Assess the morphology of the erythrocytes.
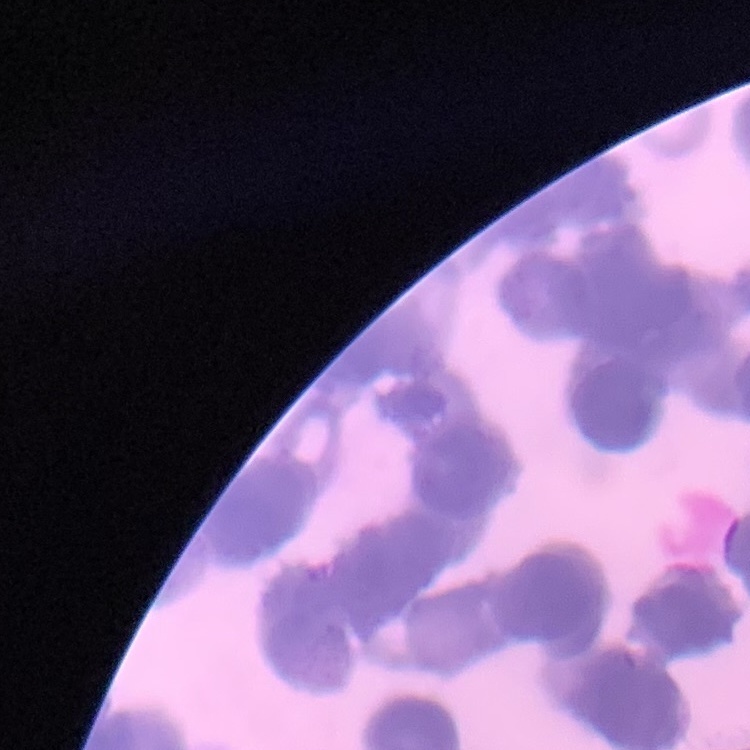

They show rouleaux formation.

Thin peripheral smear. One tile cut from a larger photomicrograph. Field's or Giemsa stain.